Evaluate for Plasmodium parasites.
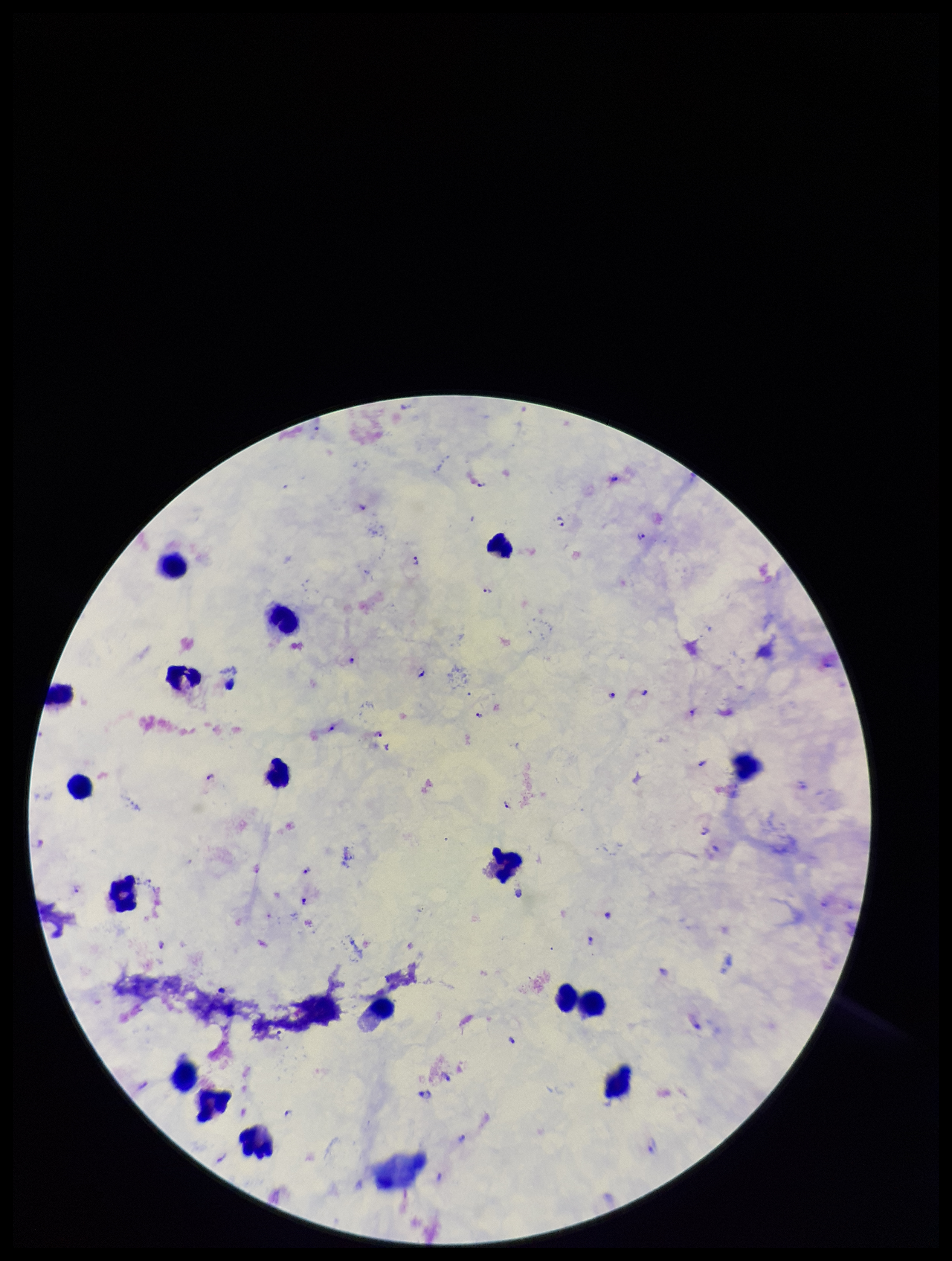

Identified.

Summary:
  - Field of view: one from this slide
  - Patient malaria status: infected
  - Species reported for this patient: Plasmodium falciparum
  - Leukocyte count: 19
  - Parasite count: 23
  - Stain: Giemsa
  - Image size: 952×1261 pixels
  - Preparation: thick blood smear
  - Capture: smartphone photograph through the microscope eyepiece